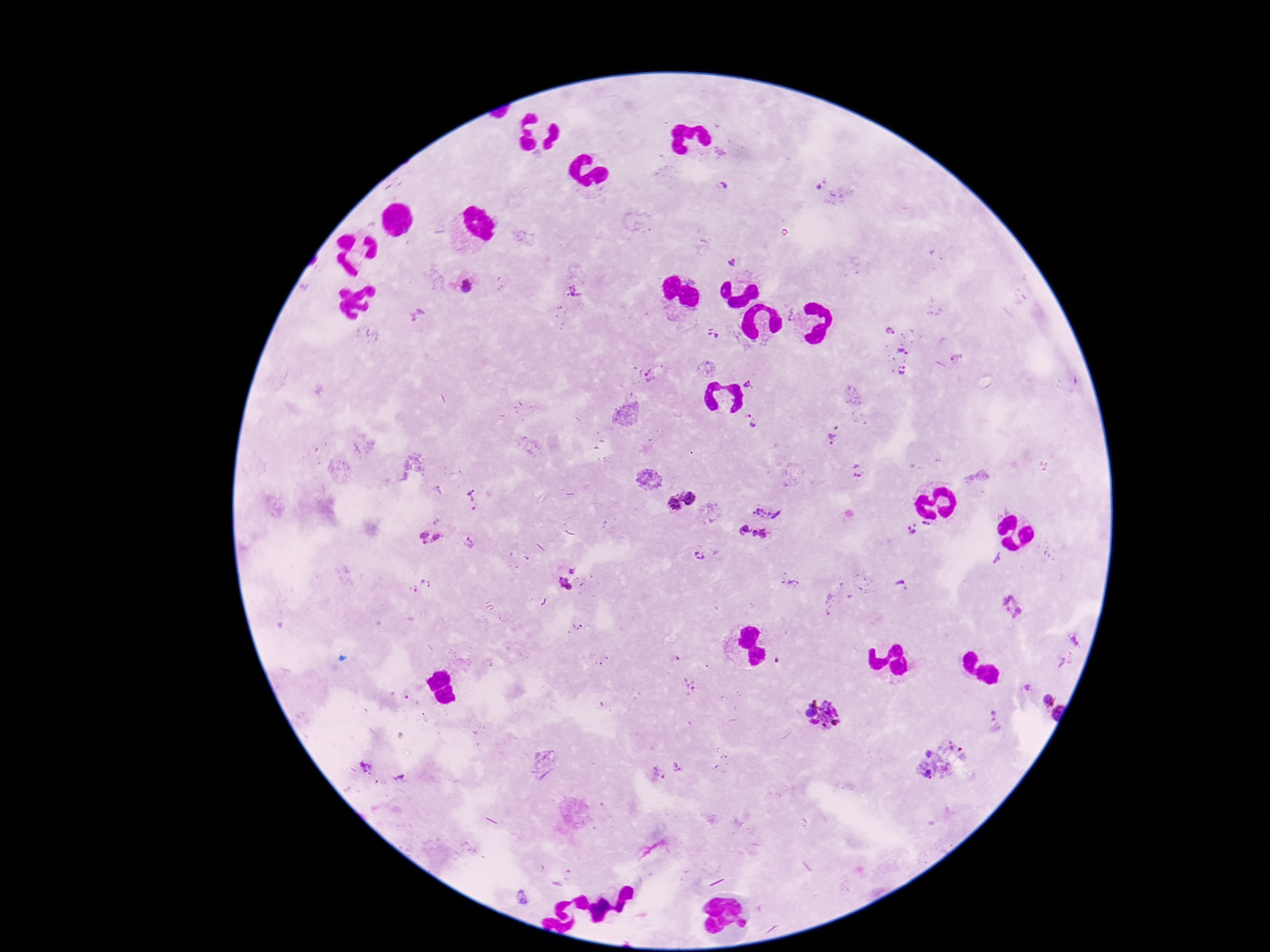

Approximate object centers, in pixels from the top-left corner.
Summary:
  - Plasmodium parasite locations: (x=724, y=185), (x=819, y=185), (x=732, y=262), (x=467, y=287), (x=575, y=293), (x=790, y=313), (x=417, y=315), (x=890, y=331), (x=713, y=333), (x=902, y=352), (x=707, y=368), (x=903, y=370), (x=650, y=376), (x=749, y=384), (x=752, y=421), (x=834, y=439), (x=857, y=469), (x=439, y=490), (x=689, y=496), (x=472, y=501), (x=673, y=503), (x=769, y=507), (x=926, y=525), (x=743, y=529), (x=912, y=531), (x=425, y=534), (x=762, y=535), (x=437, y=536), (x=426, y=542), (x=469, y=543), (x=699, y=557), (x=998, y=559), (x=572, y=570), (x=561, y=579), (x=789, y=580), (x=426, y=584), (x=901, y=586), (x=569, y=587), (x=830, y=604), (x=1014, y=605), (x=1074, y=639), (x=1060, y=661), (x=689, y=687), (x=1027, y=688), (x=1044, y=700), (x=811, y=712), (x=993, y=713), (x=1058, y=713), (x=825, y=715), (x=994, y=719), (x=928, y=754), (x=367, y=768), (x=677, y=768), (x=929, y=773), (x=658, y=774), (x=401, y=777), (x=523, y=898)
  - Magnification: 100x
  - Field of view: single
  - Patient malaria status: positive
  - Stain: Giemsa
  - Preparation: thick peripheral-blood smear
  - Capture: smartphone camera through the microscope eyepiece
  - Image size: 1270×952 pixels